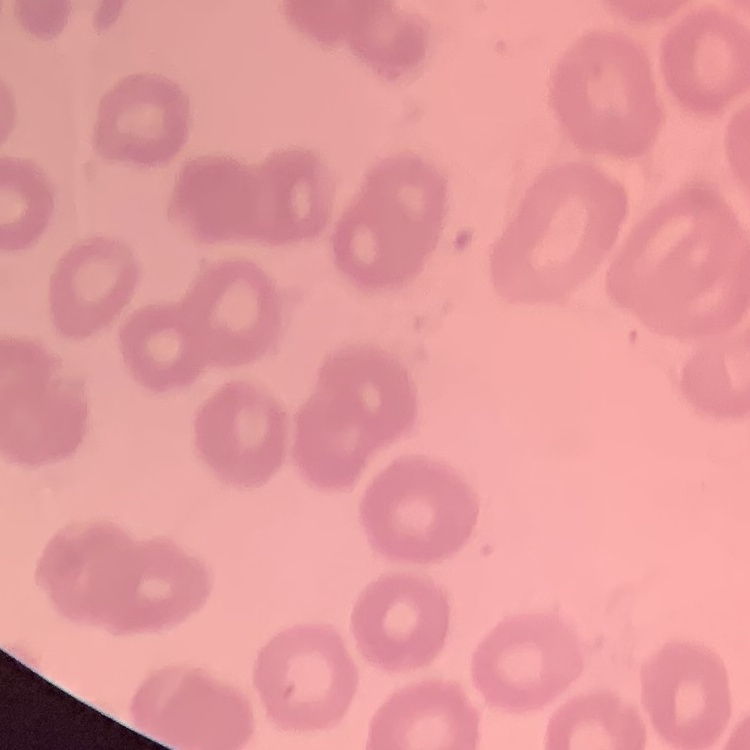
Summary:
  - Erythrocyte morphology: no rouleaux formation
  - Image type: square crop of a larger photomicrograph
  - Stain: Field's or Giemsa
  - Preparation: thin blood smear